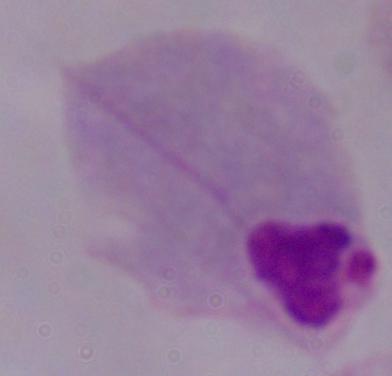
magnification = 1000x
modality = photomicrograph
identification = trichomonad